Rate the background quality.
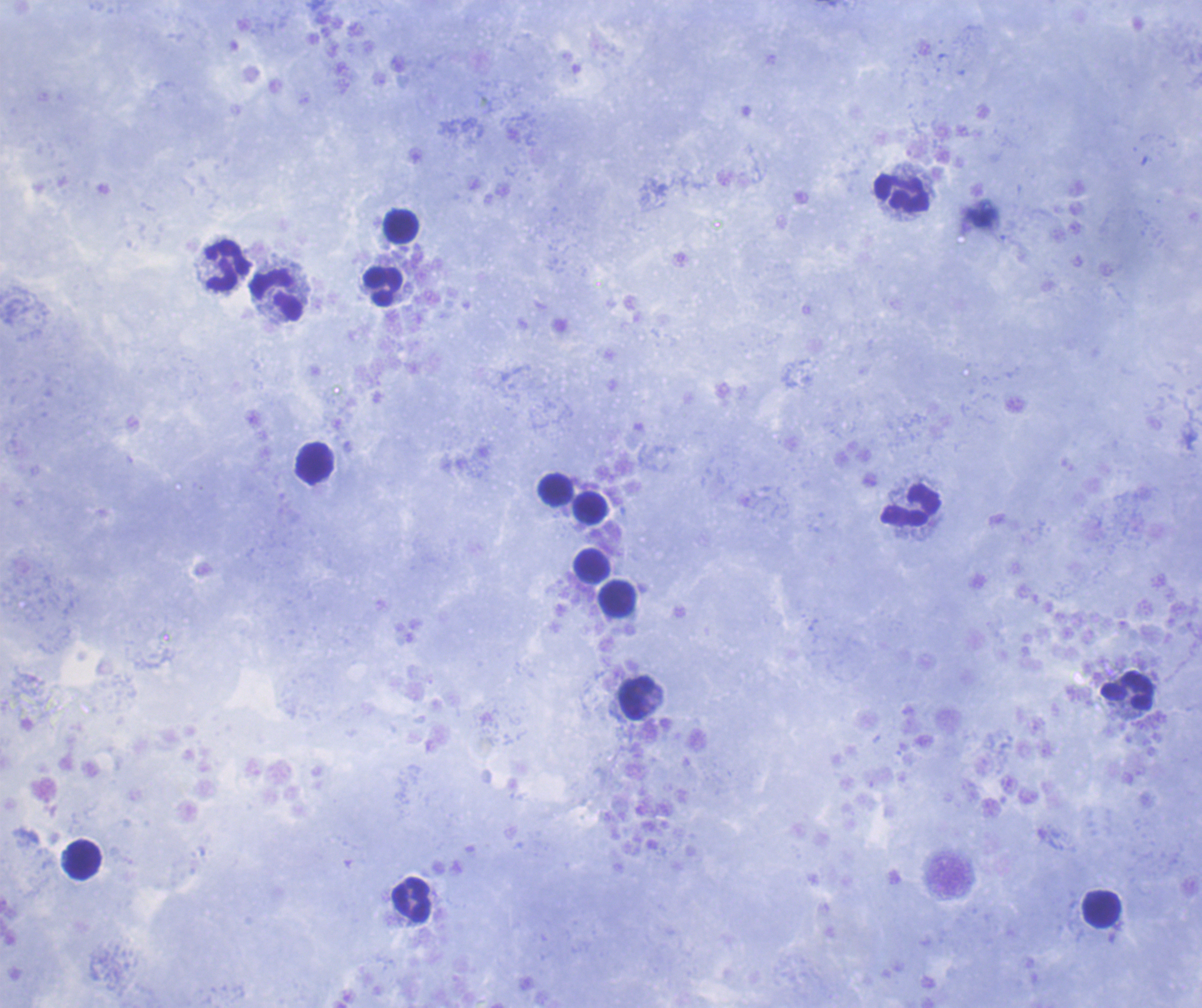
Satisfactory.

{
  "field_of_view": "one from this slide",
  "result": "negative for Plasmodium parasites",
  "image_size": "1202×1008 pixels",
  "preparation": "thick blood smear",
  "leukocyte_locations": "approximate object centers, in pixels from the top-left corner: (x=902, y=194), (x=400, y=226), (x=226, y=267), (x=382, y=287), (x=277, y=295), (x=314, y=462), (x=556, y=490), (x=911, y=506), (x=589, y=508), (x=593, y=565), (x=618, y=598), (x=1126, y=691), (x=637, y=699), (x=82, y=859), (x=411, y=902), (x=1101, y=909)",
  "stain": "Romanowsky",
  "coloration_quality": "good",
  "magnification": "100x",
  "context": "previously used in a real diagnosis"
}